Locate every blood parasite and identify its species.
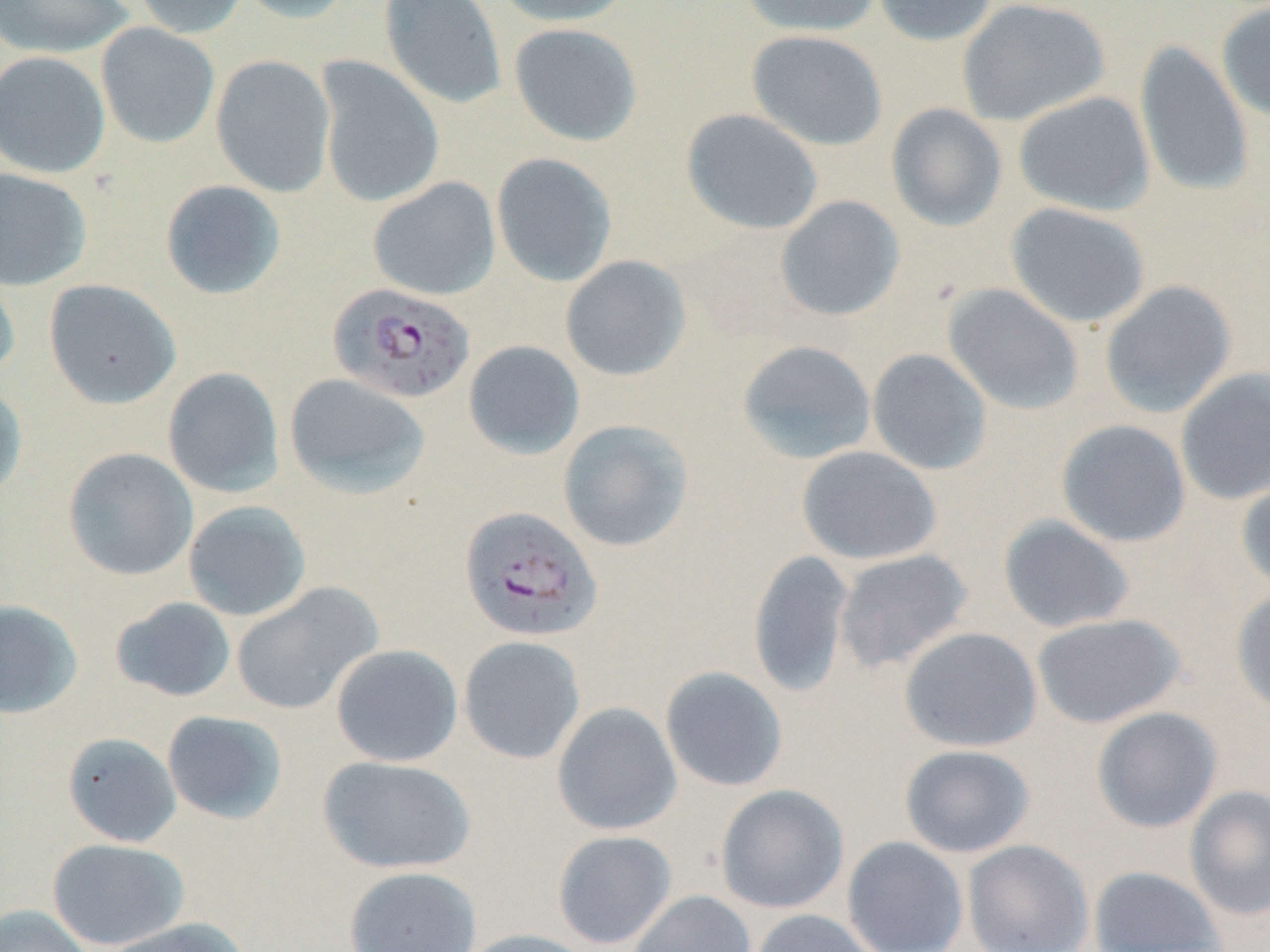
Approximate bounding boxes as (x1, y1, x2, y2) in pixels.
Plasmodium falciparum-infected red blood cells: (327, 283, 475, 405), (459, 506, 603, 643).
No Plasmodium ovale, Plasmodium malariae, Plasmodium vivax, Babesia divergens, or Trypanosoma brucei observed.

Uninfected red blood cell locations: (0, 0, 135, 59), (130, 0, 248, 38), (234, 0, 358, 24), (379, 0, 507, 110), (495, 0, 633, 27), (738, 0, 882, 37), (872, 0, 999, 47), (956, 0, 1111, 126), (1216, 2, 1270, 123), (96, 23, 219, 148), (508, 23, 642, 146), (746, 30, 888, 151), (1133, 41, 1254, 199), (0, 51, 111, 178), (211, 54, 336, 198), (313, 56, 444, 208), (1013, 91, 1155, 216), (885, 103, 1008, 232), (681, 108, 823, 235), (491, 152, 617, 287), (0, 167, 92, 290), (367, 177, 501, 301), (160, 179, 286, 300), (775, 195, 905, 322), (1004, 202, 1151, 328), (560, 255, 692, 381), (0, 258, 21, 382), (44, 279, 182, 409), (1099, 280, 1237, 419), (942, 283, 1085, 416), (736, 339, 877, 465), (462, 340, 585, 460), (866, 348, 992, 476), (1175, 366, 1270, 505), (162, 367, 284, 498), (284, 373, 430, 499), (0, 382, 28, 502), (557, 419, 694, 552), (1055, 419, 1191, 547), (795, 445, 942, 565), (63, 447, 198, 581), (1236, 469, 1270, 594), (183, 500, 311, 621), (998, 515, 1134, 633), (833, 548, 973, 673), (747, 549, 855, 699), (230, 582, 383, 715), (1231, 587, 1270, 716), (110, 596, 236, 702), (0, 599, 84, 719), (1030, 613, 1187, 728), (898, 626, 1043, 752), (458, 636, 586, 765), (331, 644, 463, 767), (660, 666, 789, 792), (551, 702, 682, 836), (1091, 706, 1223, 833), (161, 710, 288, 824), (62, 732, 181, 847), (899, 744, 1036, 858), (317, 754, 476, 875), (715, 783, 849, 914), (1183, 784, 1270, 921), (552, 830, 677, 949), (841, 835, 969, 952), (46, 837, 190, 950), (962, 839, 1094, 952), (344, 865, 482, 952), (1088, 866, 1227, 951), (628, 889, 757, 952), (0, 903, 93, 952), (749, 909, 883, 952), (101, 918, 253, 952), (457, 928, 598, 952). Slide-level diagnosis: Plasmodium falciparum. Image is 1270×952 pixels. Thin blood film. May-Grünwald-Giemsa stain. Light microscopy. Single field of view. 1000x magnification.